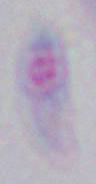
identification = Toxoplasma gondii
magnification = 1000x
modality = micrograph